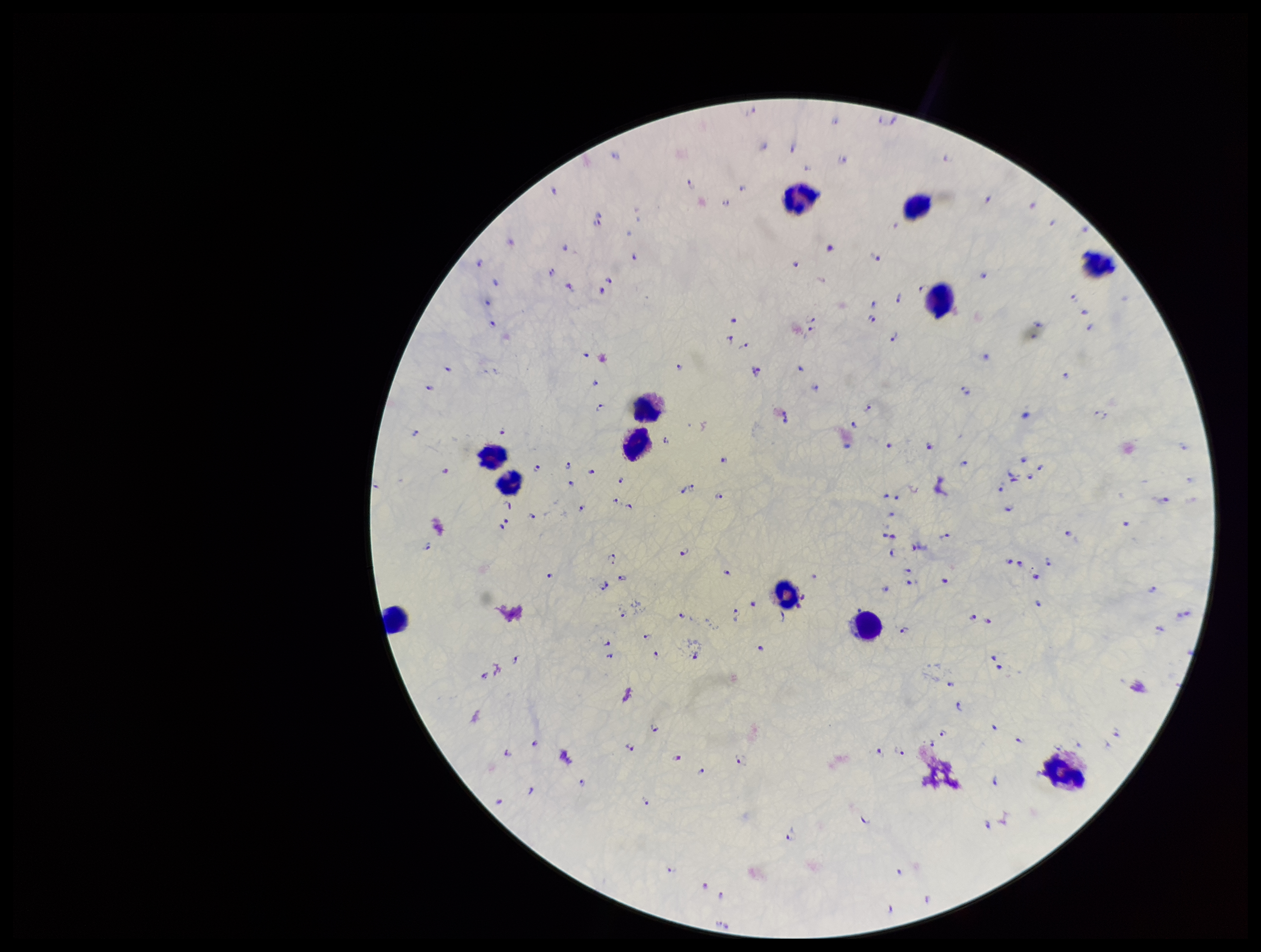

Summary:
  - Preparation: thick smear
  - Capture: smartphone photograph through the microscope eyepiece
  - Patient malaria status: positive
  - Stain: Giemsa
  - Plasmodium parasites: identified
  - Leukocyte count: 12
  - Image size: 1261×952 pixels
  - Parasite count: 188
  - Field of view: one from this slide
  - Species reported for this patient: Plasmodium falciparum